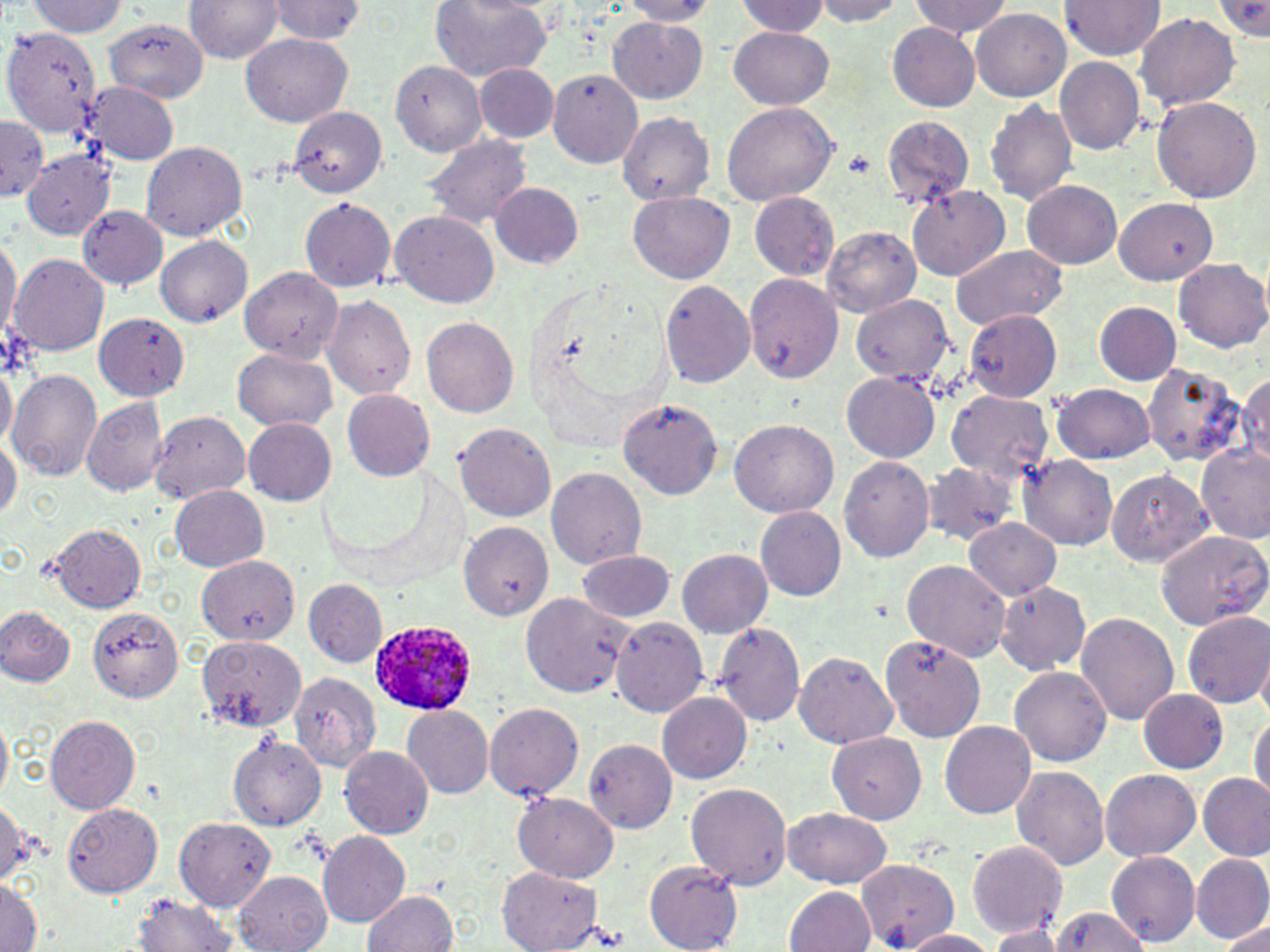

Approximate bounding boxes as [x1, y1, x2, y2] in pixels. Uninfected red blood cell locations: [184, 0, 285, 63], [814, 0, 906, 26], [1062, 0, 1165, 59], [1213, 0, 1270, 39], [25, 1, 129, 37], [265, 1, 365, 42], [430, 1, 551, 81], [734, 1, 830, 37], [910, 1, 1012, 37], [619, 2, 718, 24], [971, 8, 1070, 101], [1134, 13, 1241, 110], [609, 16, 707, 103], [101, 19, 209, 101], [887, 23, 979, 111], [729, 26, 834, 110], [2, 27, 101, 139], [239, 32, 354, 127], [1055, 56, 1145, 154], [390, 60, 485, 157], [473, 61, 561, 143], [548, 68, 643, 168], [81, 82, 178, 167], [1152, 96, 1263, 204], [985, 98, 1078, 206], [722, 101, 839, 205], [287, 106, 387, 198], [615, 112, 719, 204], [880, 115, 975, 209], [0, 118, 47, 201], [421, 133, 532, 230], [140, 142, 248, 240], [21, 148, 116, 240], [1022, 180, 1122, 268], [490, 183, 586, 268], [905, 184, 1010, 281], [747, 190, 841, 280], [628, 191, 734, 284], [299, 197, 395, 293], [1115, 197, 1217, 285], [77, 206, 167, 291], [389, 210, 500, 308], [823, 227, 920, 317], [0, 233, 19, 348], [157, 237, 251, 325], [949, 243, 1068, 331], [10, 254, 108, 357], [1173, 257, 1270, 353], [237, 267, 342, 361], [743, 273, 844, 383], [658, 279, 755, 389], [321, 294, 417, 400], [849, 294, 955, 388], [1094, 301, 1181, 385], [963, 308, 1062, 402], [93, 312, 190, 402], [422, 316, 518, 418], [232, 347, 338, 432], [0, 359, 16, 451], [1140, 364, 1248, 467], [9, 368, 99, 479], [840, 370, 940, 464], [1238, 373, 1269, 471], [1053, 383, 1156, 463], [342, 388, 435, 480], [945, 389, 1054, 486], [81, 397, 168, 496], [617, 399, 721, 499], [151, 411, 252, 504], [243, 417, 337, 507], [728, 418, 838, 516], [451, 422, 556, 521], [0, 433, 21, 522], [1197, 445, 1269, 545], [1018, 454, 1118, 549], [838, 455, 935, 562], [921, 461, 1022, 547], [546, 466, 647, 569], [1104, 468, 1212, 567], [172, 484, 268, 571], [754, 505, 846, 601], [966, 518, 1061, 601], [458, 521, 553, 619], [48, 522, 147, 611], [1153, 527, 1270, 630], [676, 548, 773, 638], [577, 549, 675, 621], [196, 553, 300, 644], [900, 559, 1013, 663], [303, 579, 387, 668], [995, 581, 1091, 676], [521, 593, 633, 699], [0, 606, 75, 686], [88, 606, 183, 703], [1182, 610, 1270, 708], [1076, 612, 1178, 725], [610, 616, 709, 718], [712, 621, 805, 726], [196, 634, 308, 732], [881, 636, 984, 743], [1255, 644, 1270, 728], [792, 650, 898, 748], [1009, 666, 1112, 766], [290, 671, 382, 772], [1138, 688, 1229, 773], [657, 691, 752, 784], [484, 702, 586, 801], [402, 704, 493, 800], [1248, 709, 1269, 807], [0, 711, 12, 802], [45, 715, 140, 813], [939, 720, 1037, 819], [827, 732, 925, 824], [230, 735, 326, 829], [583, 737, 679, 833], [340, 744, 434, 838], [1011, 767, 1110, 871], [1101, 769, 1200, 862], [1198, 772, 1270, 861], [686, 783, 792, 889], [514, 792, 618, 881], [0, 797, 35, 886], [63, 802, 162, 897], [782, 807, 892, 888], [173, 816, 277, 911], [318, 831, 410, 926], [963, 837, 1069, 938], [1106, 849, 1200, 947], [1191, 854, 1270, 943], [854, 857, 961, 948], [643, 860, 745, 951], [497, 867, 603, 952], [234, 870, 332, 952], [0, 873, 41, 952], [786, 885, 876, 952], [363, 890, 457, 951], [133, 894, 240, 951], [1048, 907, 1152, 952], [1220, 921, 1270, 950], [984, 925, 1064, 951], [899, 929, 998, 951]. Plasmodium ovale-infected red blood cell locations: [365, 620, 477, 718]. Slide-level diagnosis: Plasmodium ovale. Image is 1270×952 pixels. Light microscopy. May-Grünwald-Giemsa-stained preparation. One field of a larger specimen. Thin blood film. Captured at 1000x magnification.